Point out each malaria parasite.
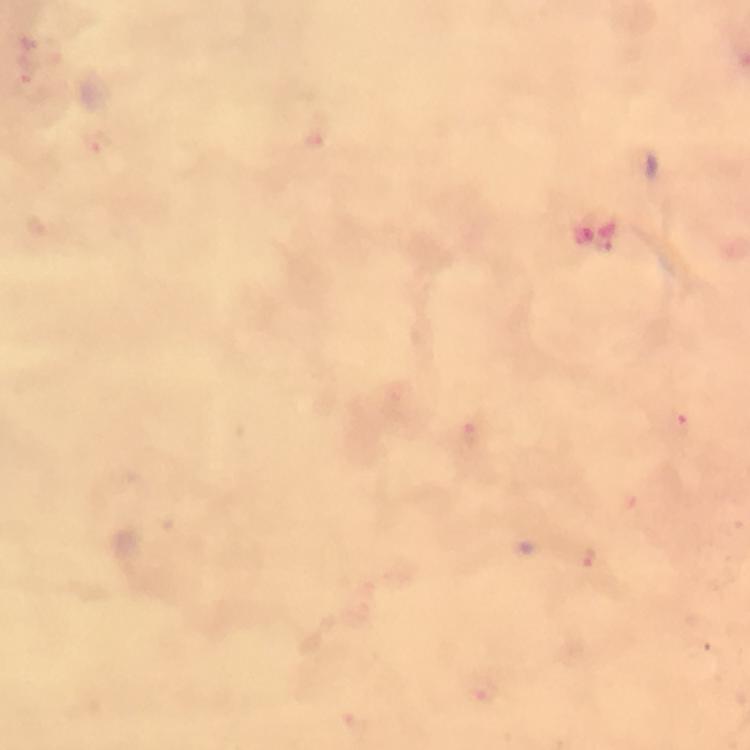

Approximate centers as (x, y) in pixels.
Malaria parasites: (28, 73), (97, 144), (602, 246), (681, 427), (471, 433), (589, 560), (482, 694).

Summary:
  - Magnification: 100x
  - Cropped from: a single field of view
  - Image size: 750×750 pixels
  - Immersion oil: applied
  - Context: from a diagnostic examination for malaria
  - Capture: smartphone mounted on the microscope
  - Preparation: thick blood smear
  - Stain: Giemsa